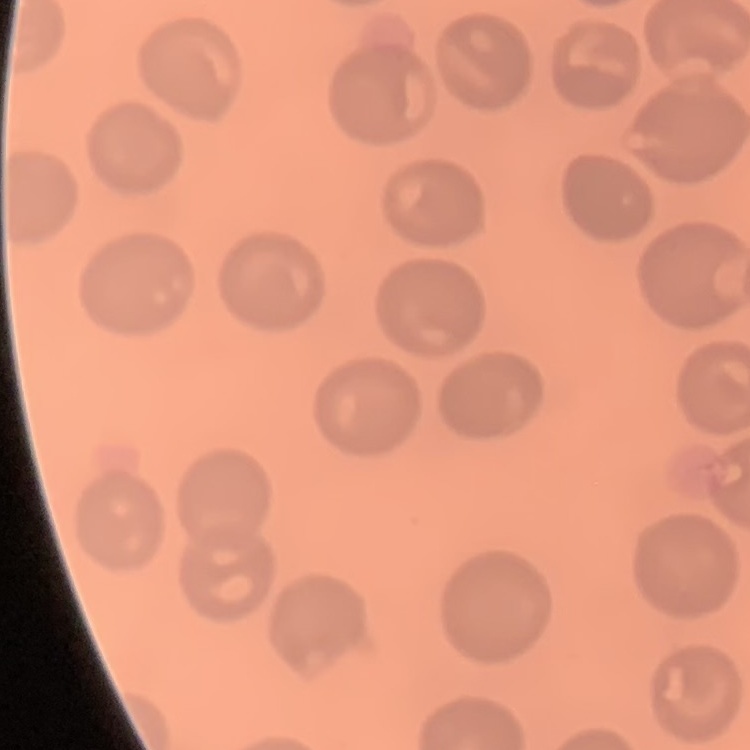 The erythrocytes show no rouleaux formation. Thin blood film. Field's or Giemsa stain. Square crop of a larger photomicrograph.